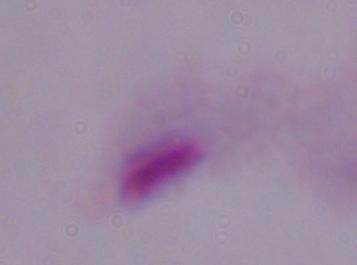

Summary:
  - Identification: trichomonad
  - Magnification: 1000x
  - Modality: micrograph